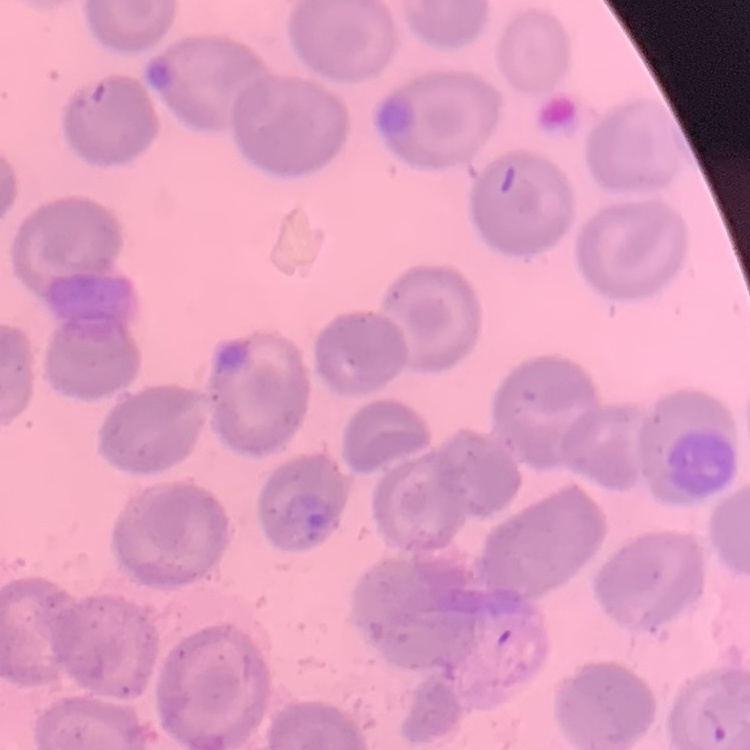

red blood cell morphology = no rouleaux formation
preparation = thin blood film
image type = square crop of a larger photomicrograph
stain = Field's or Giemsa